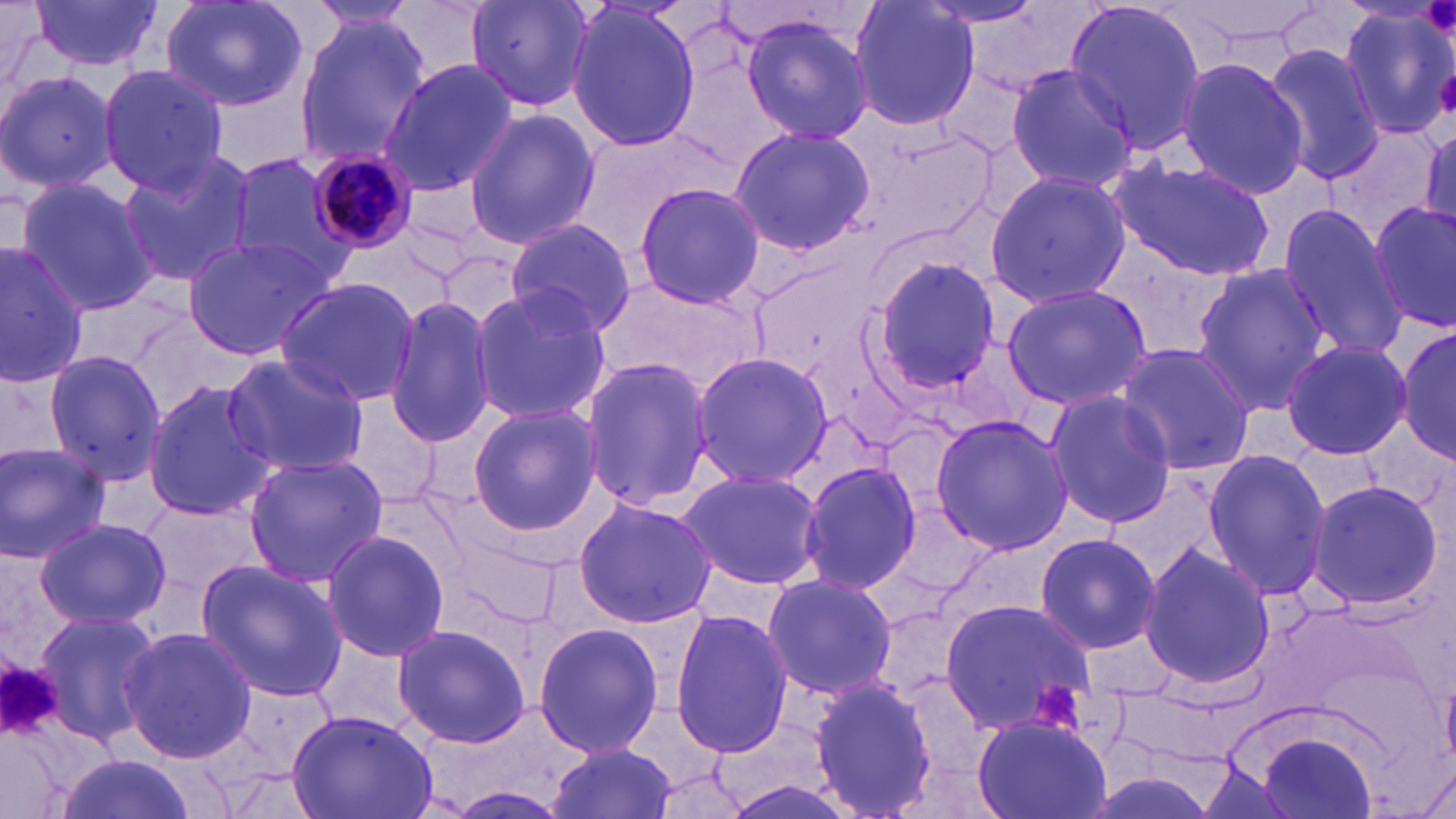
{
  "slide_level_diagnosis": "Plasmodium malariae",
  "image_size": "1456×819 pixels",
  "preparation": "thin blood film",
  "modality": "light microscopy",
  "stain": "May-Grünwald-Giemsa",
  "magnification": "1000x",
  "plasmodium_malariae_infected_red_blood_cell_locations": "approximate bounding boxes as (x1, y1, x2, y2) in pixels: (306, 148, 424, 253)",
  "field_of_view": "one of a larger specimen",
  "platelet_locations": "approximate bounding boxes as (x1, y1, x2, y2) in pixels: (1422, 0, 1456, 44), (1436, 68, 1454, 115), (1, 662, 65, 740), (1027, 679, 1082, 734)",
  "uninfected_red_blood_cell_locations": "approximate bounding boxes as (x1, y1, x2, y2) in pixels: (1, 0, 57, 99), (29, 0, 162, 73), (160, 0, 308, 113), (466, 0, 596, 112), (1166, 0, 1327, 51), (304, 1, 423, 35), (847, 1, 982, 133), (1062, 1, 1211, 152), (563, 4, 703, 151), (1336, 6, 1456, 141), (737, 11, 877, 144), (291, 13, 431, 170), (1262, 44, 1389, 185), (1174, 57, 1310, 200), (377, 59, 517, 198), (98, 64, 227, 195), (1004, 64, 1138, 192), (0, 68, 120, 195), (463, 107, 600, 250), (1418, 124, 1455, 237), (729, 126, 878, 254), (114, 147, 259, 288), (225, 151, 360, 285), (1106, 155, 1279, 282), (985, 169, 1131, 307), (14, 176, 160, 318), (631, 180, 766, 310), (1369, 197, 1456, 334), (1278, 205, 1406, 359), (504, 218, 635, 339), (181, 235, 341, 358), (0, 243, 89, 388), (868, 253, 1003, 399), (1190, 261, 1332, 413), (274, 278, 421, 407), (467, 284, 612, 427), (1000, 284, 1150, 412), (384, 297, 497, 449), (1397, 320, 1454, 466), (1280, 337, 1413, 461), (1112, 342, 1253, 476), (40, 348, 168, 485), (691, 350, 833, 491), (221, 352, 368, 477), (581, 355, 715, 512), (142, 380, 277, 523), (1044, 388, 1176, 529), (339, 394, 444, 511), (466, 402, 602, 536), (929, 413, 1071, 556), (0, 442, 110, 564), (1200, 449, 1333, 602), (242, 453, 388, 586), (797, 460, 921, 596), (676, 468, 824, 590), (1103, 469, 1234, 584), (1306, 480, 1444, 609), (139, 494, 265, 599), (572, 496, 716, 630), (32, 517, 171, 632), (320, 529, 450, 662), (1032, 531, 1163, 654), (1138, 543, 1276, 690), (194, 558, 347, 701), (761, 572, 897, 700), (939, 597, 1098, 736), (30, 607, 161, 747), (670, 608, 795, 759), (393, 621, 533, 751), (532, 622, 663, 757), (119, 628, 258, 761), (805, 673, 939, 819), (286, 709, 440, 819), (971, 714, 1111, 819), (1250, 728, 1384, 819), (545, 742, 678, 819), (53, 753, 199, 819)"
}